Give the position of every Plasmodium parasite.
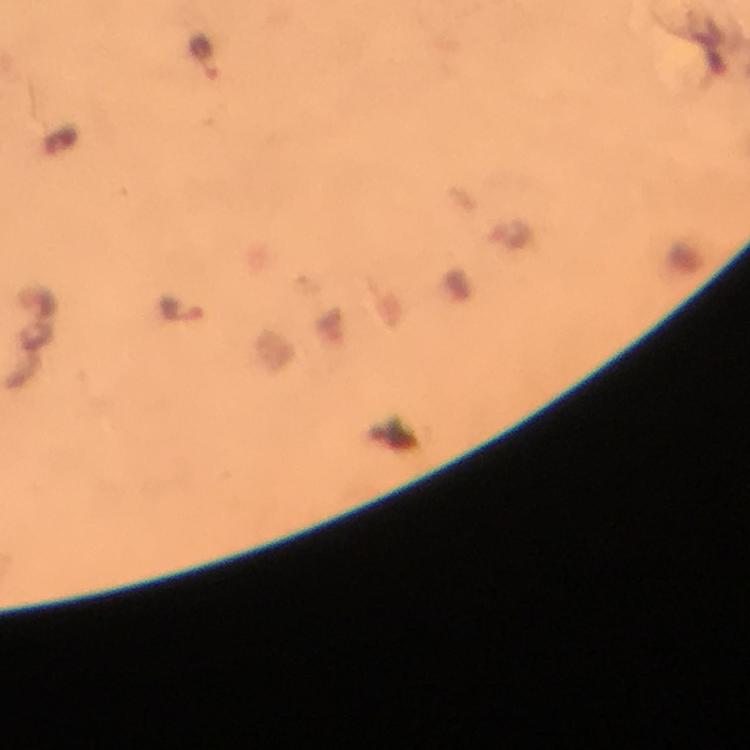
Approximate centers as (x, y) in pixels.
Plasmodium parasites: (203, 58), (182, 311).

Summary:
  - Capture: smartphone mounted on the microscope
  - Cropped from: one field of view
  - Context: from a diagnostic examination for malaria
  - Image size: 750×750 pixels
  - Stain: Giemsa
  - Immersion oil: used
  - Magnification: 100x
  - Preparation: thick blood smear